Identify the parasite.
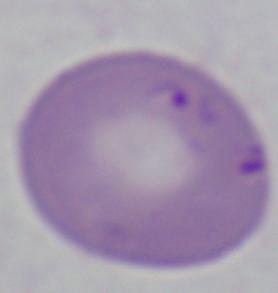

Babesia.

Summary:
  - Modality: micrograph
  - Magnification: 1000x